Name the parasite shown.
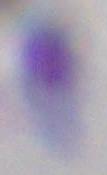
This is Toxoplasma gondii.

Micrograph. 1000x magnification.